Describe the morphology of the erythrocytes.
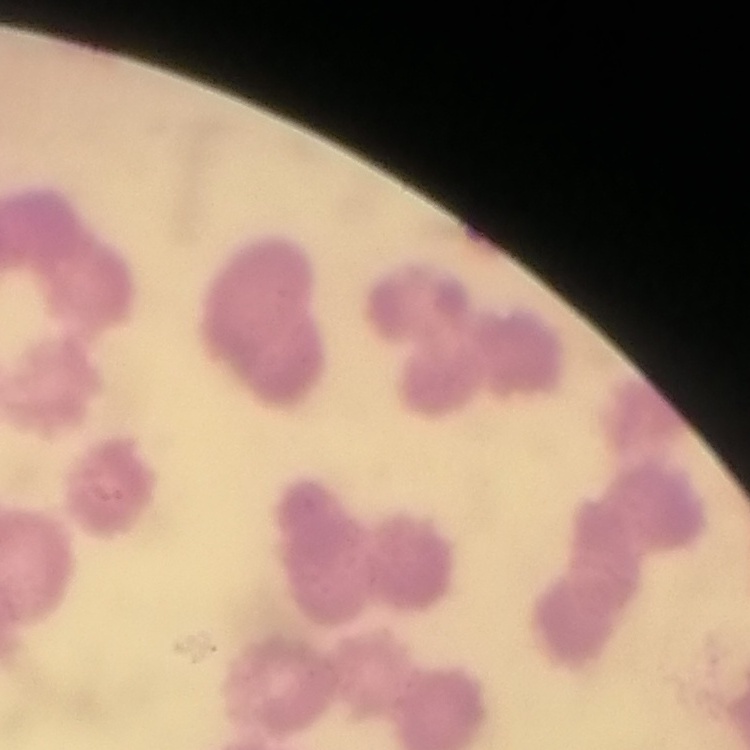

They show rouleaux formation.

Square crop of a larger photomicrograph. Field's or Giemsa stain. Thin blood smear.